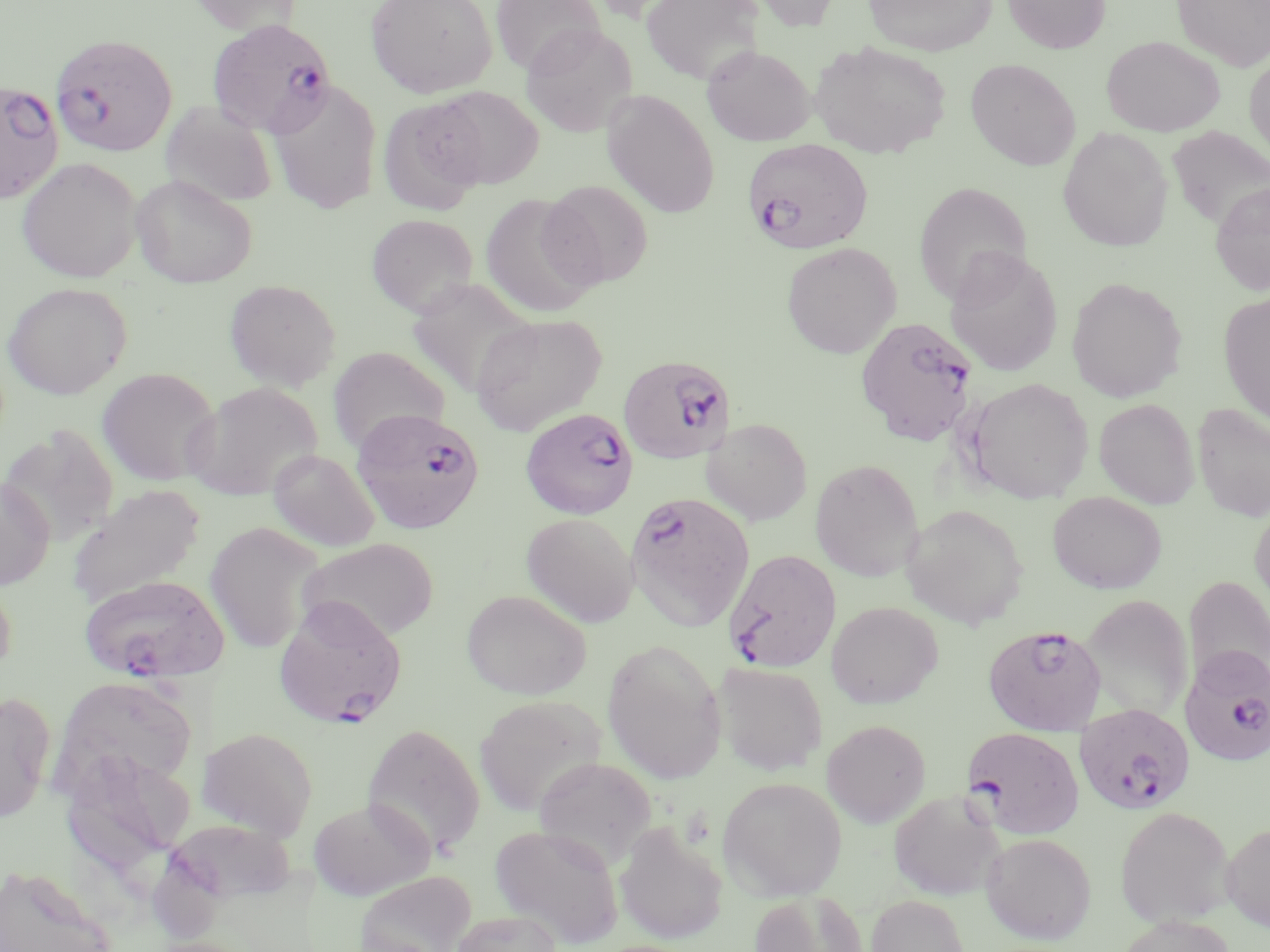

Approximate bounding boxes as (x1, y1, x2, y2) in pixels. Uninfected red blood cell locations: (186, 0, 303, 36), (366, 0, 497, 98), (490, 0, 605, 76), (640, 0, 766, 84), (746, 0, 843, 31), (862, 0, 998, 56), (1002, 0, 1111, 54), (1172, 0, 1270, 71), (521, 23, 638, 137), (1101, 35, 1225, 136), (809, 39, 952, 158), (701, 44, 816, 146), (1244, 52, 1270, 166), (965, 58, 1081, 170), (269, 80, 383, 214), (429, 86, 544, 189), (603, 90, 720, 217), (377, 97, 489, 215), (161, 101, 277, 208), (1167, 126, 1270, 231), (1057, 127, 1173, 252), (16, 157, 142, 283), (131, 175, 258, 288), (540, 180, 654, 288), (912, 181, 1032, 304), (1211, 182, 1270, 295), (479, 192, 603, 318), (366, 213, 478, 317), (781, 242, 901, 358), (944, 246, 1064, 377), (1066, 276, 1188, 403), (224, 279, 342, 391), (1, 282, 132, 400), (1218, 291, 1270, 425), (471, 313, 606, 435), (326, 346, 450, 454), (96, 367, 221, 487), (959, 377, 1094, 504), (184, 382, 322, 501), (1094, 398, 1200, 509), (1192, 403, 1270, 522), (702, 418, 813, 526), (1, 426, 119, 546), (268, 449, 381, 552), (809, 458, 924, 581), (0, 476, 55, 591), (67, 483, 206, 607), (1048, 491, 1167, 594), (1249, 503, 1270, 611), (901, 504, 1029, 629), (521, 512, 639, 627), (205, 523, 323, 653), (297, 537, 439, 643), (0, 571, 17, 683), (1183, 575, 1270, 691), (461, 589, 592, 700), (1080, 594, 1193, 721), (826, 601, 943, 708), (602, 638, 727, 783), (714, 661, 828, 775), (53, 675, 198, 795), (0, 691, 56, 823), (474, 695, 607, 816), (821, 719, 931, 827), (363, 722, 485, 858), (198, 727, 318, 840), (61, 749, 195, 873), (534, 756, 657, 869), (717, 775, 848, 900), (888, 790, 1005, 900), (307, 796, 434, 901), (1114, 806, 1235, 927), (164, 817, 298, 904), (1221, 821, 1270, 931), (615, 822, 728, 945), (489, 823, 624, 947), (981, 832, 1097, 944), (0, 863, 116, 952), (354, 870, 477, 952), (748, 890, 869, 952), (866, 895, 970, 952), (451, 910, 562, 952), (1114, 915, 1239, 952). Plasmodium falciparum-infected red blood cell locations: (207, 18, 338, 139), (51, 34, 177, 156), (0, 81, 65, 204), (742, 136, 875, 253), (855, 316, 979, 445), (619, 354, 736, 464), (351, 407, 484, 535), (520, 407, 639, 519), (627, 496, 759, 634), (724, 548, 842, 674), (76, 573, 231, 684), (273, 598, 408, 728), (984, 624, 1107, 736), (1180, 645, 1270, 767), (1074, 703, 1195, 816), (962, 726, 1085, 839). Slide-level diagnosis: Plasmodium falciparum. Optical microscopy. Image is 1270×952 pixels. 1000x magnification. Single field of view. Thin blood film. May-Grünwald-Giemsa stain.